Report the malaria status of this cell.
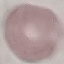
It is uninfected.

Photographed with a smartphone camera at the microscope eyepiece. Automatically extracted cell patch, resized to 64 × 64 pixels. Thin blood film. Giemsa-stained preparation.